Assess this cell for malaria.
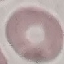

Uninfected.

preparation = thin smear
stain = Giemsa
capture = smartphone camera at the microscope eyepiece
image type = automatically extracted cell patch, resized to 64 × 64 pixels